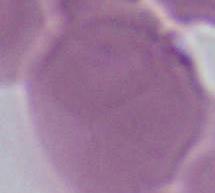
1000x magnification. Photomicrograph. An erythrocyte is seen.